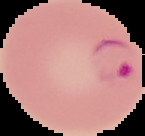

From a thin blood film. Malaria status: parasitized. Image is 145×136 pixels. The area outside the segmented cell region is set to black.